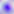

Summary:
  - Modality: photomicrograph
  - Identification: Toxoplasma gondii
  - Magnification: 400x